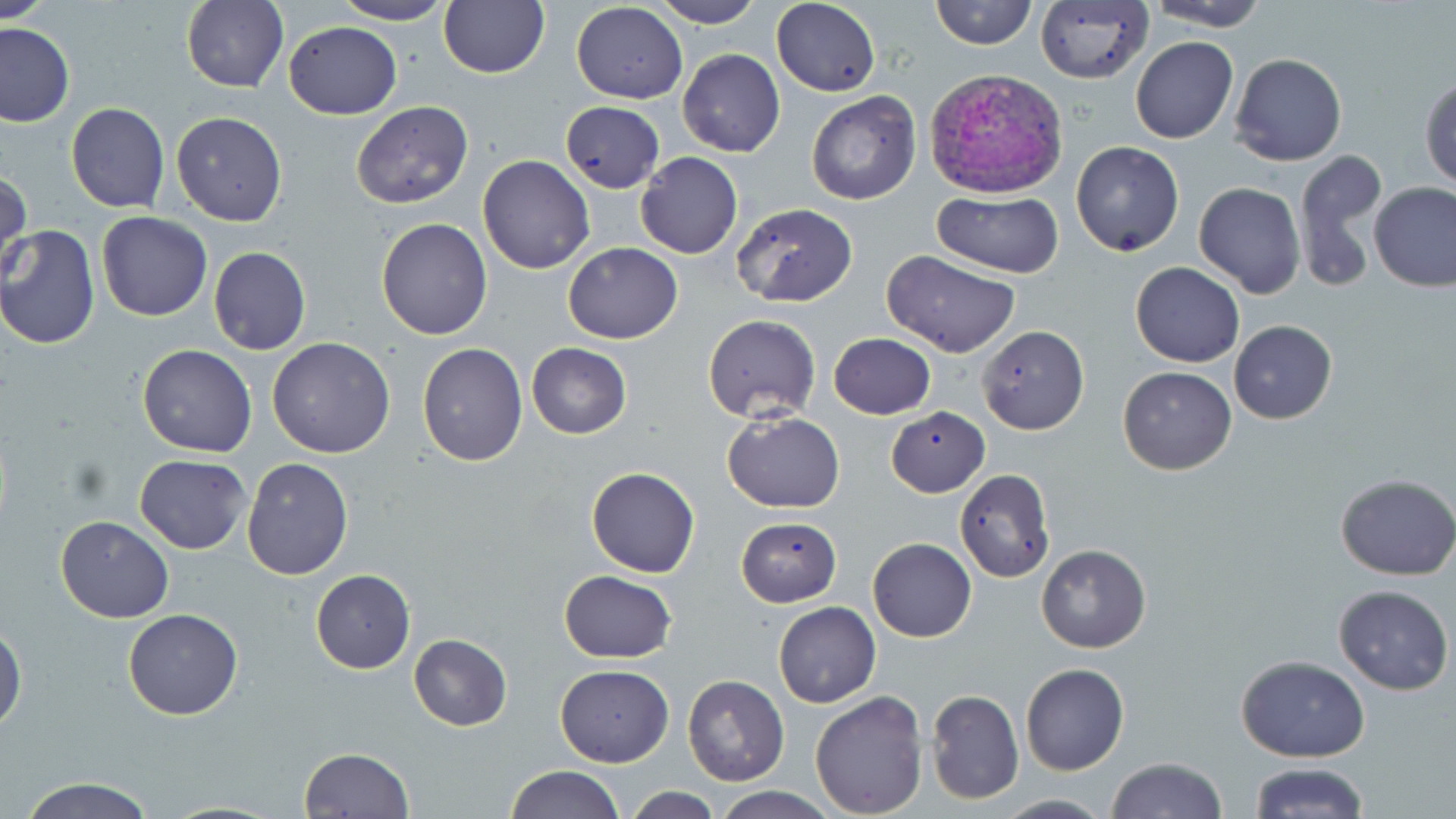
Approximate bounding boxes as named x1/y1/x2/y2 corners in pixels. Plasmodium vivax-infected red blood cell locations: (x1=924, y1=67, x2=1068, y2=200). Uninfected red blood cell locations: (x1=0, y1=0, x2=52, y2=23), (x1=182, y1=0, x2=288, y2=92), (x1=331, y1=0, x2=456, y2=25), (x1=647, y1=0, x2=765, y2=27), (x1=771, y1=0, x2=879, y2=96), (x1=930, y1=0, x2=1036, y2=49), (x1=1034, y1=0, x2=1156, y2=86), (x1=1142, y1=0, x2=1272, y2=32), (x1=438, y1=1, x2=550, y2=78), (x1=571, y1=2, x2=687, y2=105), (x1=283, y1=20, x2=403, y2=120), (x1=0, y1=22, x2=74, y2=127), (x1=1130, y1=36, x2=1239, y2=144), (x1=677, y1=48, x2=785, y2=157), (x1=1229, y1=53, x2=1346, y2=167), (x1=1420, y1=75, x2=1455, y2=190), (x1=806, y1=90, x2=922, y2=206), (x1=350, y1=101, x2=475, y2=210), (x1=560, y1=101, x2=666, y2=195), (x1=65, y1=102, x2=170, y2=214), (x1=170, y1=112, x2=288, y2=225), (x1=1070, y1=141, x2=1184, y2=256), (x1=1293, y1=147, x2=1389, y2=294), (x1=636, y1=151, x2=743, y2=259), (x1=477, y1=155, x2=595, y2=274), (x1=0, y1=168, x2=32, y2=274), (x1=1370, y1=181, x2=1456, y2=292), (x1=1193, y1=182, x2=1305, y2=300), (x1=933, y1=192, x2=1061, y2=277), (x1=730, y1=202, x2=856, y2=307), (x1=96, y1=212, x2=213, y2=322), (x1=374, y1=217, x2=492, y2=340), (x1=0, y1=225, x2=100, y2=350), (x1=563, y1=242, x2=683, y2=344), (x1=209, y1=246, x2=311, y2=356), (x1=883, y1=250, x2=1022, y2=358), (x1=1130, y1=263, x2=1244, y2=367), (x1=701, y1=314, x2=820, y2=423), (x1=1229, y1=321, x2=1337, y2=424), (x1=978, y1=325, x2=1088, y2=435), (x1=828, y1=333, x2=935, y2=420), (x1=267, y1=337, x2=397, y2=458), (x1=527, y1=342, x2=631, y2=438), (x1=417, y1=343, x2=527, y2=466), (x1=138, y1=345, x2=256, y2=458), (x1=1117, y1=365, x2=1236, y2=475), (x1=886, y1=407, x2=991, y2=496), (x1=723, y1=411, x2=844, y2=514), (x1=135, y1=455, x2=252, y2=554), (x1=242, y1=456, x2=353, y2=579), (x1=586, y1=467, x2=699, y2=578), (x1=954, y1=468, x2=1056, y2=582), (x1=1335, y1=472, x2=1456, y2=579), (x1=56, y1=516, x2=174, y2=622), (x1=735, y1=516, x2=841, y2=606), (x1=868, y1=537, x2=977, y2=641), (x1=1036, y1=544, x2=1151, y2=653), (x1=310, y1=570, x2=416, y2=673), (x1=557, y1=570, x2=678, y2=662), (x1=1333, y1=584, x2=1453, y2=695), (x1=773, y1=602, x2=880, y2=707), (x1=122, y1=608, x2=242, y2=720), (x1=0, y1=624, x2=25, y2=733), (x1=408, y1=633, x2=511, y2=730), (x1=1236, y1=655, x2=1370, y2=762), (x1=1020, y1=663, x2=1129, y2=776), (x1=554, y1=664, x2=674, y2=766), (x1=683, y1=675, x2=788, y2=785), (x1=925, y1=688, x2=1024, y2=805), (x1=810, y1=690, x2=929, y2=818), (x1=300, y1=747, x2=414, y2=818), (x1=1105, y1=757, x2=1229, y2=818), (x1=1248, y1=763, x2=1369, y2=819), (x1=504, y1=766, x2=625, y2=819), (x1=18, y1=777, x2=157, y2=819), (x1=625, y1=786, x2=722, y2=818), (x1=710, y1=786, x2=839, y2=819), (x1=993, y1=794, x2=1111, y2=818). Slide-level diagnosis: Plasmodium vivax. Image is 1456×819 pixels. Light microscopy. Thin blood smear. May-Grünwald-Giemsa stain. One field of a larger specimen. Captured at 1000x magnification.